Describe the morphology of the red blood cells.
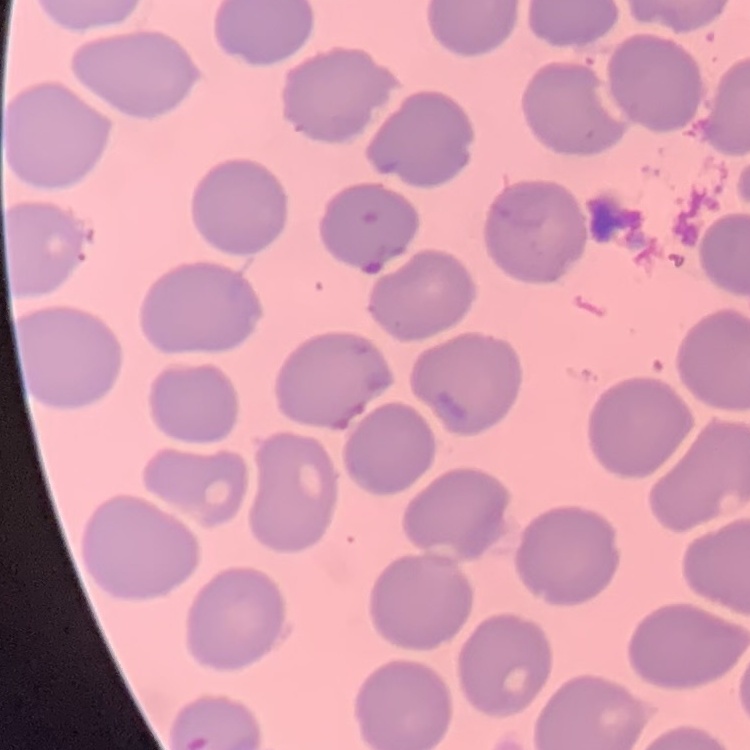
No rouleaux formation.

Summary:
  - Image type: square crop of a larger photomicrograph
  - Preparation: thin peripheral smear
  - Stain: Field's or Giemsa